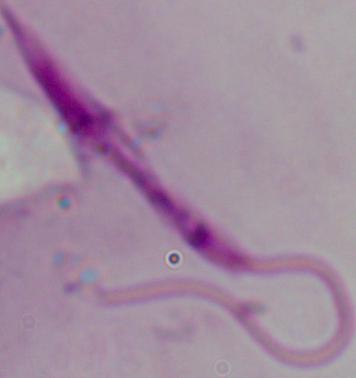
Summary:
  - Identification: Leishmania
  - Modality: micrograph
  - Magnification: 1000x